Name the cell type shown.
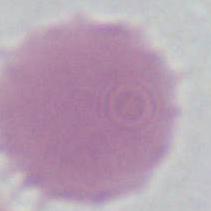
This is an erythrocyte.

magnification: 1000x
modality: photomicrograph